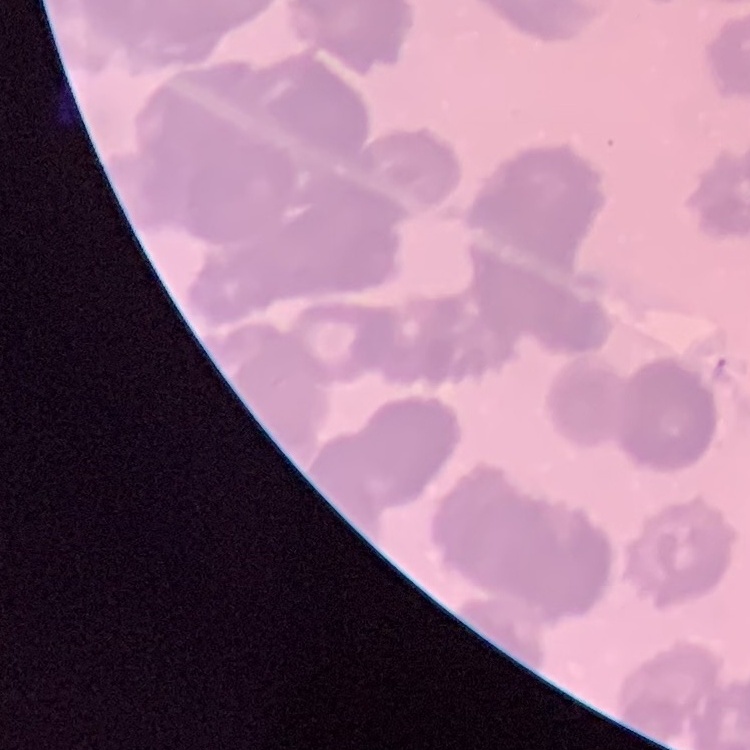
red blood cell morphology = rouleaux formation
stain = Field's or Giemsa
image type = square crop of a larger photomicrograph
preparation = thin peripheral smear